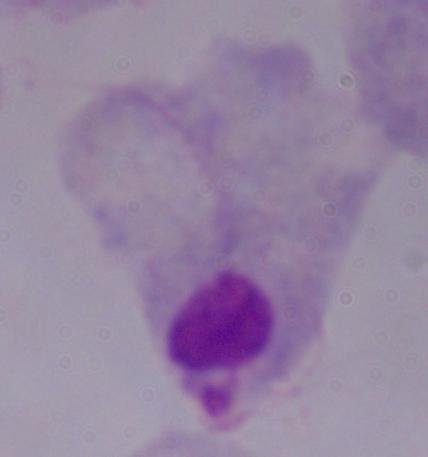
1000x magnification. A trichomonad is shown. Micrograph.